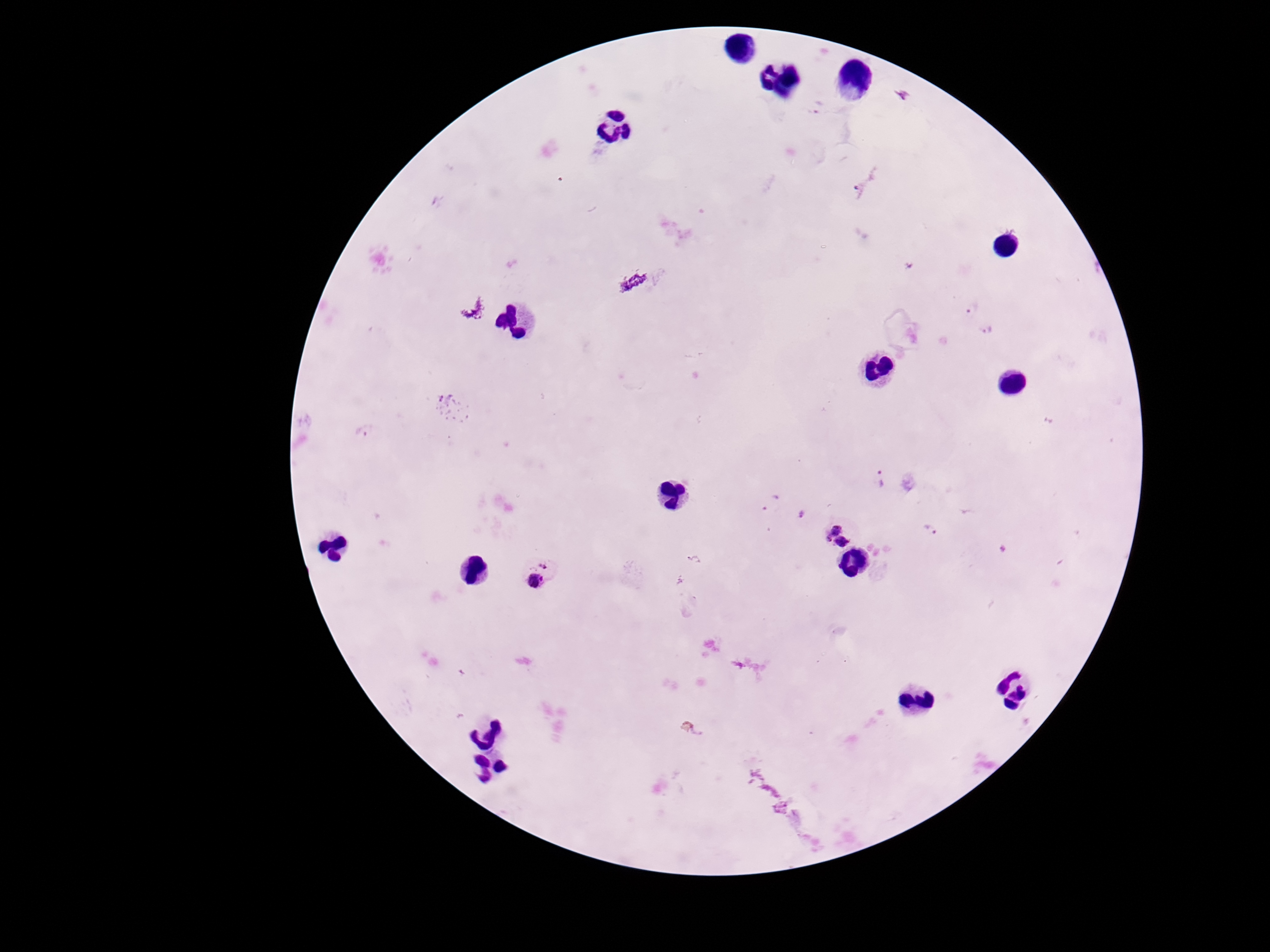
stain = Giemsa
capture = smartphone camera through the microscope eyepiece
field of view = single
image size = 1270×952 pixels
Plasmodium parasite locations = approximate centers as (x, y) in pixels: (902, 96), (818, 107), (859, 189), (633, 283), (972, 310), (988, 331), (365, 431), (880, 478), (769, 502), (801, 514), (930, 530), (837, 537), (542, 574)
preparation = thick blood film
patient malaria status = infected
magnification = 100x